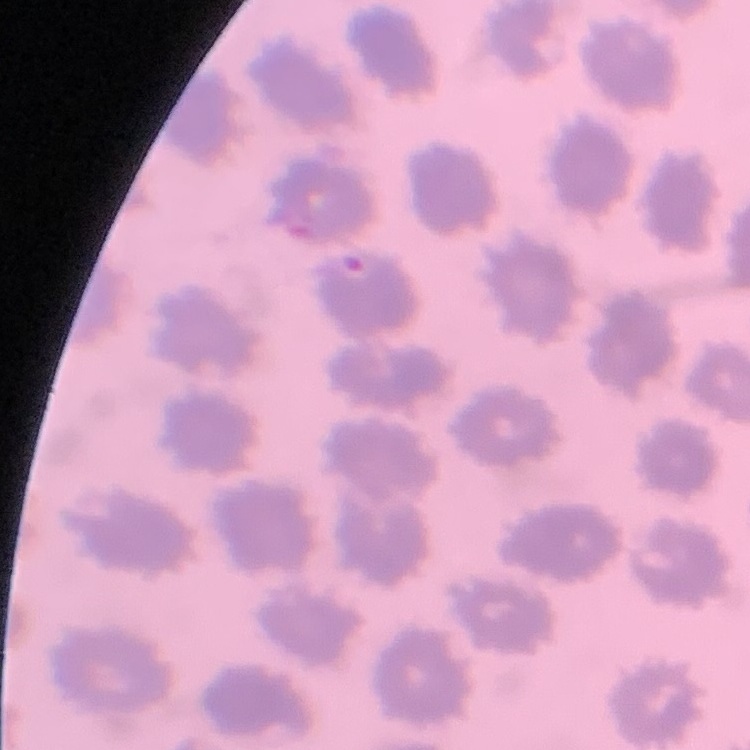 The red blood cells show no rouleaux formation. Stained with either Field's or Giemsa. One tile cut from a larger photomicrograph. Thin peripheral smear.